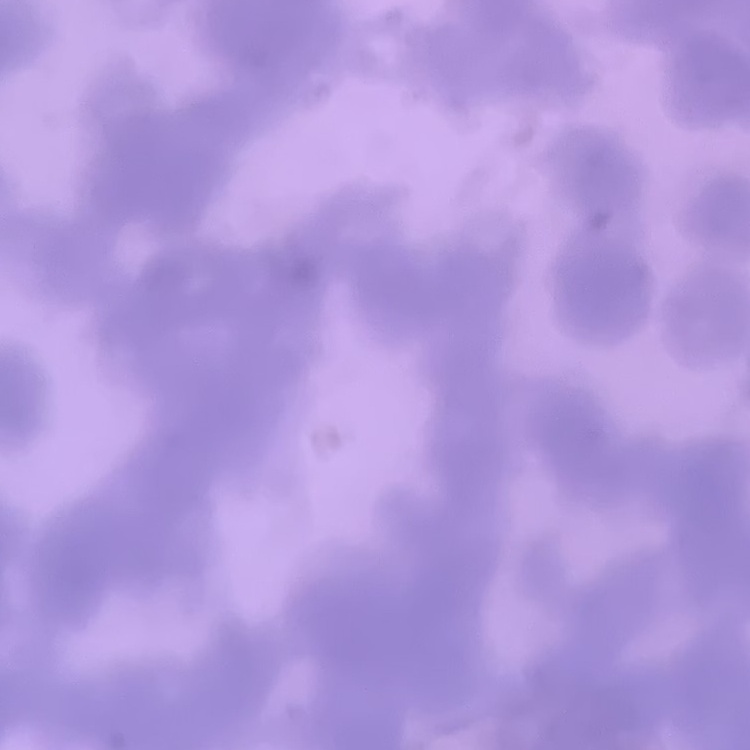

The erythrocytes exhibit rouleaux formation. One tile cut from a larger photomicrograph. Stained with either Field's or Giemsa. Thin blood smear.